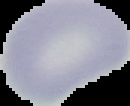

From a thin blood film. Result: no malaria parasites detected. Image is 130×106 pixels. The area outside the segmented cell region is set to black.